State which parasite is depicted.
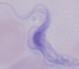
This is a trypanosome.

Summary:
  - Modality: photomicrograph
  - Magnification: 1000x